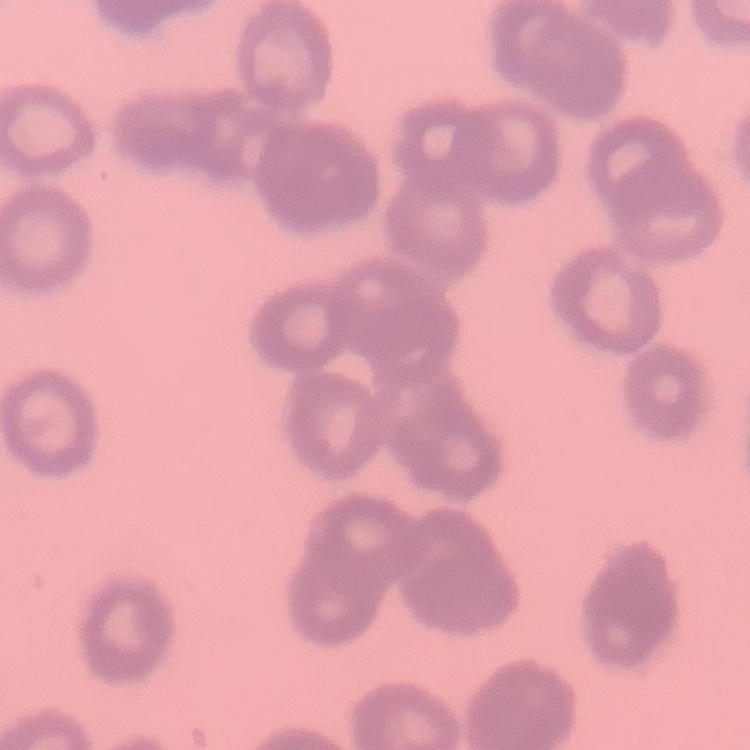

Summary:
  - Erythrocyte morphology: rouleaux formation
  - Image type: one tile cut from a larger photomicrograph
  - Preparation: thin blood film
  - Stain: Field's or Giemsa